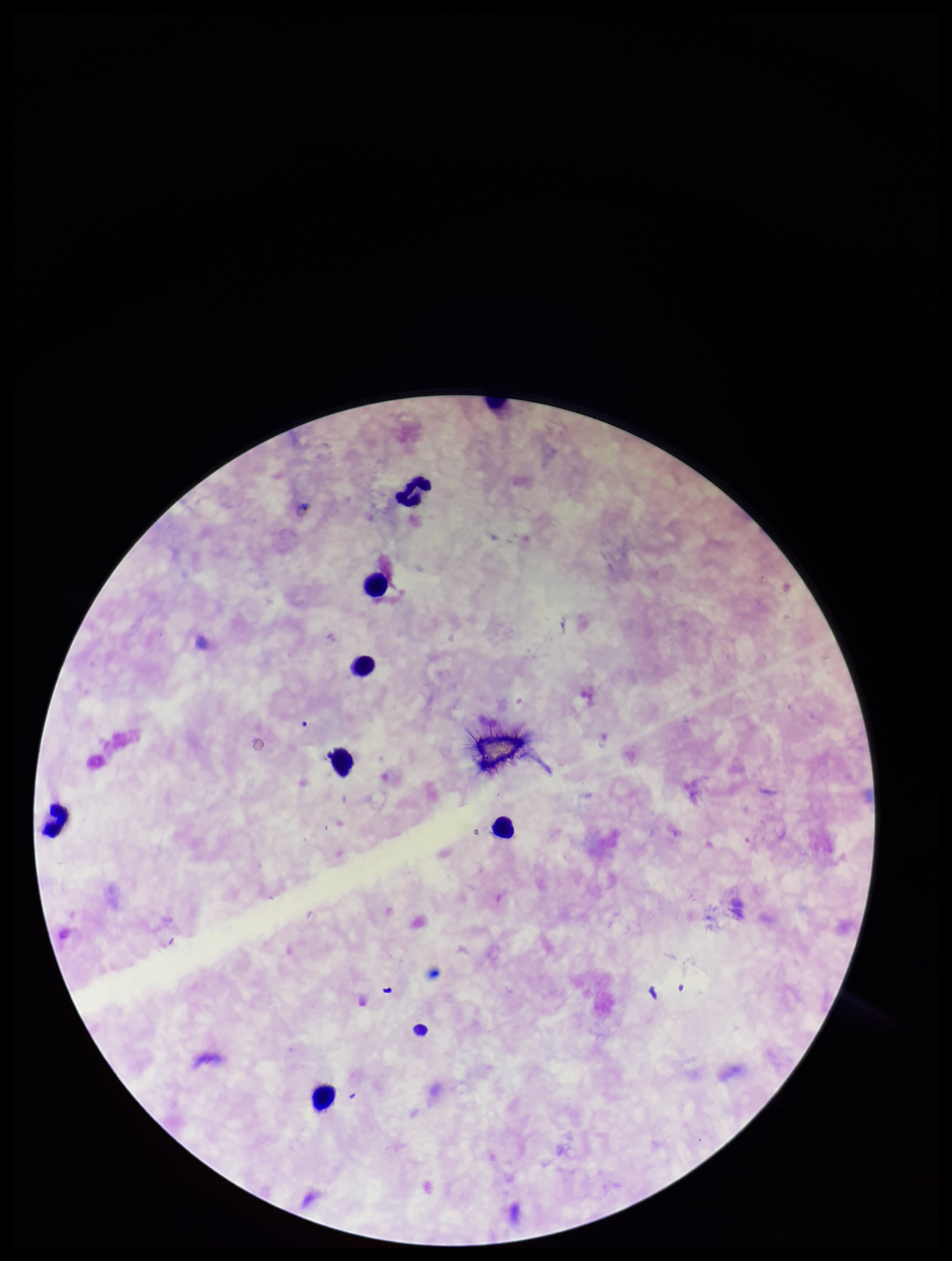

Summary:
  - Capture: smartphone photograph through the microscope eyepiece
  - Stain: Giemsa
  - Plasmodium parasites: none identified
  - Patient malaria status: negative
  - Leukocyte count: 7
  - Image size: 952×1261 pixels
  - Field of view: one from this slide
  - Parasite count: 0
  - Preparation: thick